State the blood parasite species.
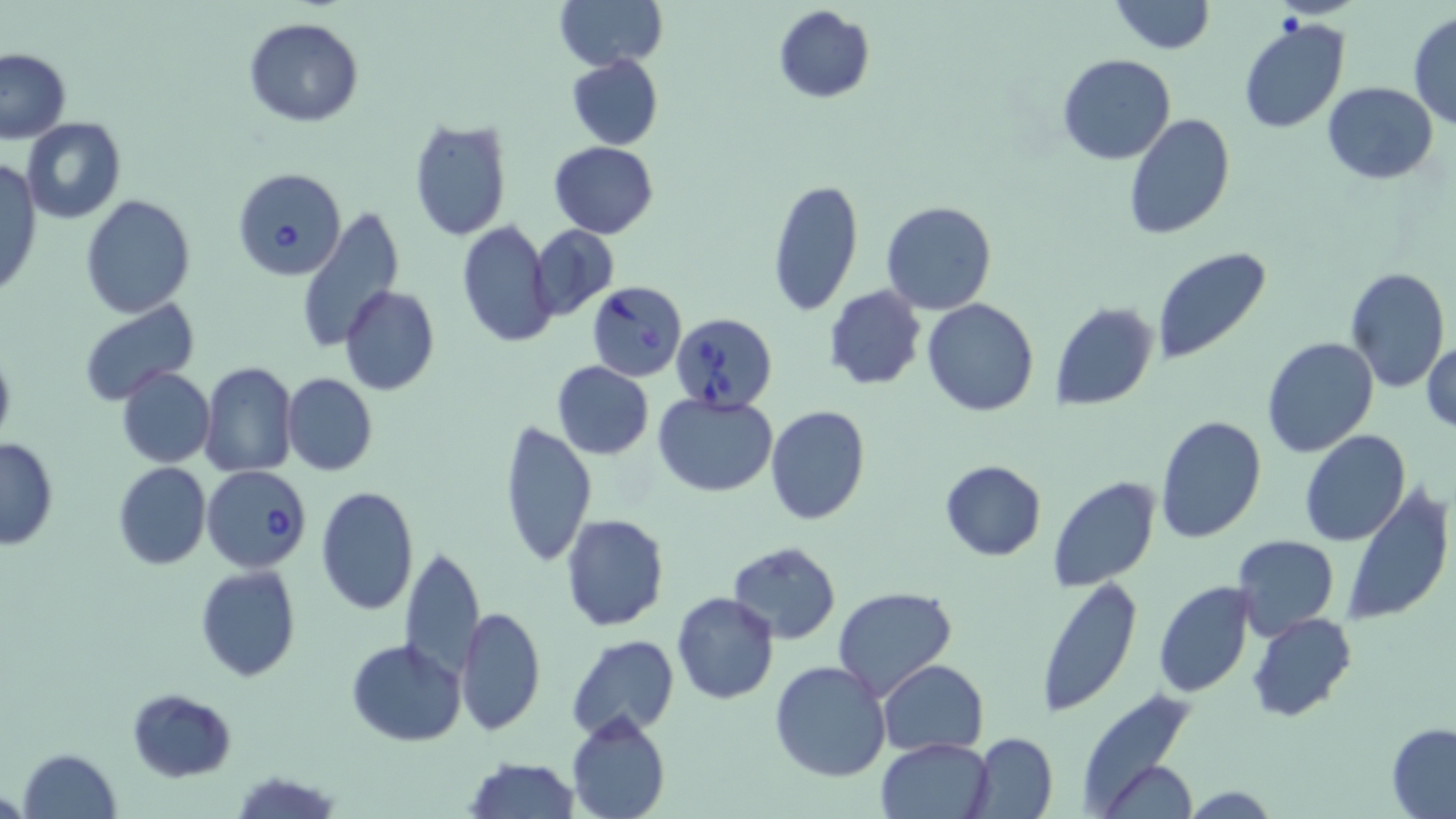

Babesia divergens.

Approximate bounding boxes as (x1, y1, x2, y2) in pixels. Babesia divergens-infected red blood cell locations: (231, 167, 347, 281), (587, 280, 688, 382), (672, 312, 781, 413), (202, 465, 312, 572). Uninfected red blood cell locations: (552, 0, 667, 71), (1110, 0, 1215, 54), (772, 5, 875, 104), (1408, 12, 1455, 129), (1237, 16, 1352, 134), (245, 17, 363, 127), (1, 47, 72, 145), (1057, 53, 1176, 166), (567, 54, 663, 150), (1321, 83, 1439, 183), (1122, 114, 1236, 241), (20, 116, 127, 224), (407, 118, 512, 242), (549, 141, 658, 238), (0, 160, 42, 301), (768, 177, 864, 316), (79, 195, 195, 317), (881, 200, 996, 315), (295, 206, 407, 354), (457, 221, 558, 349), (529, 225, 618, 318), (1152, 249, 1271, 366), (1344, 267, 1450, 394), (823, 285, 926, 390), (340, 286, 439, 397), (79, 299, 200, 404), (923, 299, 1039, 417), (1049, 303, 1159, 411), (1262, 337, 1379, 457), (1421, 337, 1455, 435), (0, 341, 16, 452), (551, 360, 654, 459), (199, 362, 298, 477), (116, 366, 215, 468), (282, 373, 377, 475), (653, 393, 777, 495), (764, 404, 872, 526), (1155, 414, 1267, 542), (499, 418, 597, 569), (1300, 431, 1411, 546), (1, 439, 59, 549), (939, 460, 1047, 560), (112, 461, 211, 570), (1046, 477, 1162, 590), (316, 484, 419, 616), (1341, 484, 1455, 627), (561, 514, 669, 632), (1232, 535, 1339, 639), (726, 541, 841, 643), (400, 544, 484, 681), (194, 566, 300, 681), (1034, 575, 1142, 719), (1153, 581, 1255, 699), (832, 586, 957, 701), (672, 592, 780, 705), (457, 608, 546, 735), (1248, 613, 1357, 723), (566, 634, 679, 741), (347, 637, 467, 746), (878, 659, 988, 756), (769, 661, 892, 783), (128, 687, 236, 780), (1081, 707, 1205, 819), (567, 713, 670, 818), (1387, 725, 1456, 816), (966, 733, 1059, 819), (877, 736, 995, 819), (17, 748, 121, 819), (463, 757, 581, 817), (1102, 760, 1197, 819), (1184, 785, 1280, 817). Light microscopy. May-Grünwald-Giemsa stain. One field of a larger specimen. Image is 1456×819 pixels. Thin blood film. 1000x magnification.